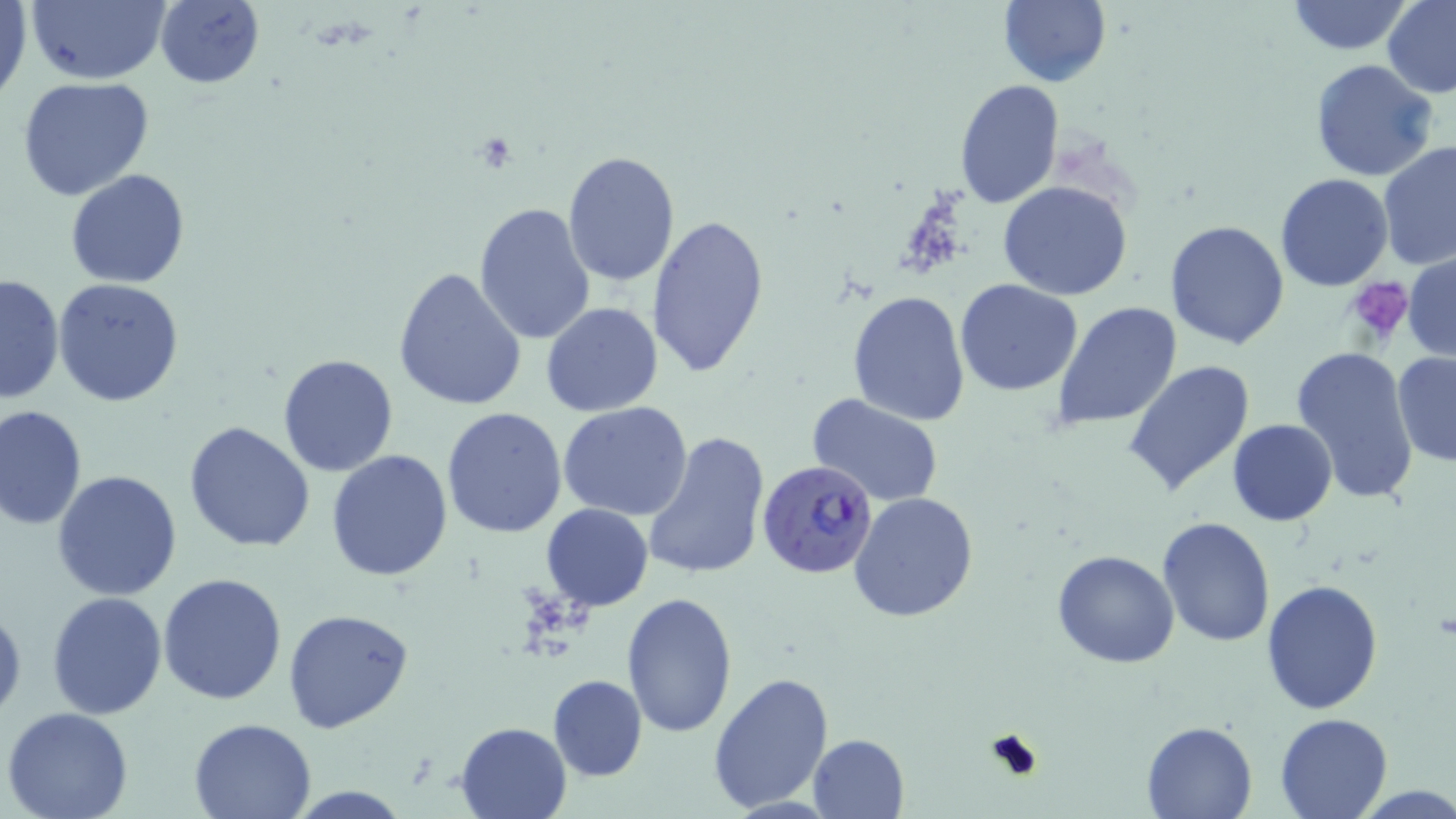
Approximate bounding boxes as (x1,y1)-(x2,y2) corner pairs in pixels. Uninfected red blood cell locations: (0,0)-(32,108), (24,0)-(172,85), (154,0)-(266,88), (996,1)-(1112,88), (1285,1)-(1414,55), (1382,2)-(1456,98), (1309,58)-(1439,184), (18,78)-(155,201), (954,78)-(1064,210), (1377,140)-(1456,272), (563,150)-(680,287), (65,168)-(190,288), (1275,173)-(1394,292), (996,181)-(1134,300), (474,201)-(595,344), (645,212)-(770,379), (1165,221)-(1291,351), (1404,252)-(1456,365), (392,267)-(527,414), (1,272)-(66,404), (53,278)-(186,407), (953,279)-(1084,396), (846,289)-(971,426), (541,302)-(665,418), (1051,302)-(1183,431), (1290,344)-(1420,504), (1392,349)-(1456,468), (278,354)-(400,476), (1122,359)-(1254,497), (806,392)-(946,507), (559,402)-(694,519), (0,406)-(88,532), (440,406)-(567,540), (1228,418)-(1339,525), (183,421)-(315,554), (640,428)-(771,582), (326,449)-(453,581), (53,469)-(183,600), (847,491)-(979,624), (542,503)-(653,610), (1157,516)-(1275,648), (1051,549)-(1179,669), (158,571)-(289,706), (1261,579)-(1385,717), (46,591)-(167,722), (622,592)-(738,737), (0,598)-(25,723), (284,607)-(415,735), (708,672)-(835,813), (547,674)-(646,781), (2,708)-(134,819), (1273,712)-(1394,819), (186,717)-(317,819), (455,720)-(572,818), (1140,721)-(1258,818), (807,733)-(908,817). Platelet locations: (473,132)-(519,172), (1346,279)-(1415,346), (984,725)-(1045,782). Plasmodium falciparum-infected red blood cell locations: (755,460)-(881,578). Slide-level diagnosis: Plasmodium falciparum. Image is 1456×819 pixels. 1000x magnification. Thin blood film. May-Grünwald-Giemsa-stained preparation. Light microscopy. Single field of view.